Name the blood parasite species.
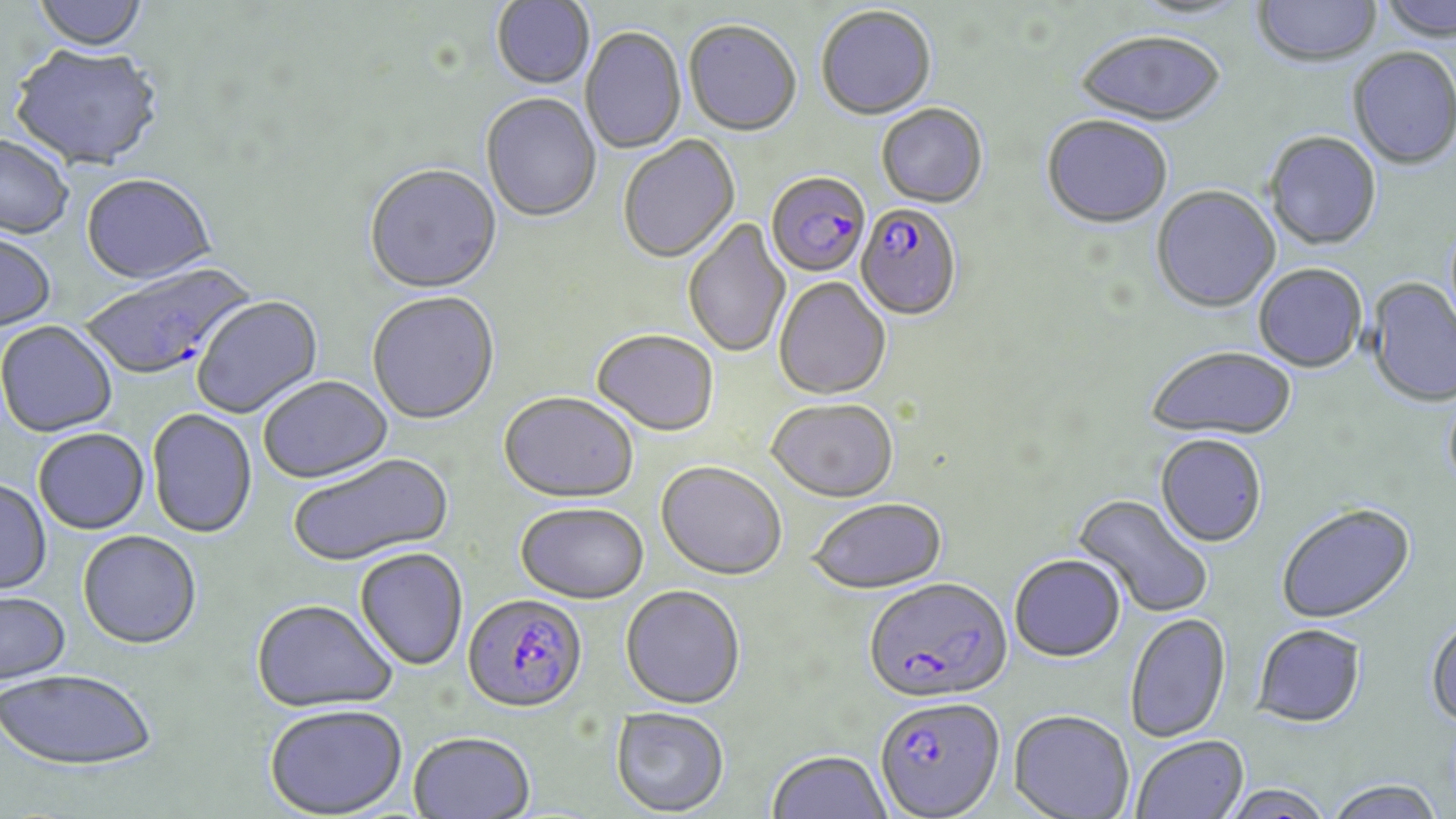

Plasmodium falciparum.

uninfected red blood cell locations = approximate bounding boxes as named x1/y1/x2/y2 corners in pixels: (x1=30, y1=0, x2=151, y2=54), (x1=1131, y1=0, x2=1248, y2=22), (x1=1252, y1=0, x2=1381, y2=69), (x1=1379, y1=0, x2=1456, y2=43), (x1=491, y1=1, x2=595, y2=91), (x1=815, y1=6, x2=936, y2=120), (x1=683, y1=20, x2=801, y2=137), (x1=580, y1=27, x2=686, y2=153), (x1=1076, y1=34, x2=1226, y2=129), (x1=9, y1=48, x2=164, y2=174), (x1=1348, y1=48, x2=1456, y2=172), (x1=480, y1=94, x2=602, y2=224), (x1=877, y1=103, x2=988, y2=208), (x1=1041, y1=117, x2=1173, y2=231), (x1=1264, y1=133, x2=1382, y2=252), (x1=0, y1=135, x2=74, y2=242), (x1=618, y1=136, x2=740, y2=264), (x1=364, y1=166, x2=501, y2=296), (x1=80, y1=176, x2=217, y2=288), (x1=1151, y1=187, x2=1280, y2=315), (x1=683, y1=219, x2=791, y2=359), (x1=0, y1=234, x2=56, y2=334), (x1=1253, y1=265, x2=1368, y2=373), (x1=774, y1=277, x2=891, y2=400), (x1=1366, y1=277, x2=1456, y2=409), (x1=367, y1=293, x2=500, y2=427), (x1=192, y1=296, x2=324, y2=420), (x1=0, y1=322, x2=118, y2=439), (x1=591, y1=330, x2=719, y2=437), (x1=1145, y1=347, x2=1298, y2=441), (x1=258, y1=377, x2=393, y2=485), (x1=499, y1=393, x2=638, y2=504), (x1=766, y1=398, x2=899, y2=502), (x1=147, y1=409, x2=258, y2=539), (x1=33, y1=429, x2=149, y2=535), (x1=1155, y1=435, x2=1267, y2=548), (x1=287, y1=454, x2=454, y2=568), (x1=657, y1=461, x2=787, y2=581), (x1=0, y1=481, x2=52, y2=596), (x1=1073, y1=493, x2=1214, y2=619), (x1=809, y1=496, x2=947, y2=593), (x1=515, y1=502, x2=649, y2=604), (x1=1277, y1=503, x2=1416, y2=625), (x1=77, y1=531, x2=202, y2=651), (x1=354, y1=548, x2=468, y2=672), (x1=1009, y1=554, x2=1126, y2=663), (x1=621, y1=585, x2=746, y2=709), (x1=0, y1=592, x2=72, y2=687), (x1=251, y1=599, x2=398, y2=714), (x1=1124, y1=613, x2=1231, y2=742), (x1=1425, y1=616, x2=1456, y2=730), (x1=1251, y1=623, x2=1368, y2=728), (x1=0, y1=670, x2=157, y2=773), (x1=263, y1=704, x2=408, y2=817), (x1=610, y1=706, x2=730, y2=816), (x1=1008, y1=709, x2=1134, y2=819), (x1=408, y1=733, x2=535, y2=819), (x1=1130, y1=735, x2=1249, y2=819), (x1=767, y1=749, x2=892, y2=819), (x1=1322, y1=778, x2=1447, y2=819), (x1=1217, y1=784, x2=1336, y2=819)
Plasmodium falciparum-infected red blood cell locations = approximate bounding boxes as named x1/y1/x2/y2 corners in pixels: (x1=766, y1=172, x2=870, y2=278), (x1=856, y1=202, x2=962, y2=321), (x1=80, y1=261, x2=260, y2=384), (x1=863, y1=577, x2=1013, y2=703), (x1=462, y1=595, x2=587, y2=715), (x1=873, y1=695, x2=1005, y2=818)
magnification = 1000x
preparation = thin blood smear
stain = May-Grünwald-Giemsa
modality = light microscopy
image size = 1456×819 pixels
field of view = one of a larger specimen